Locate every blood parasite and identify its species.
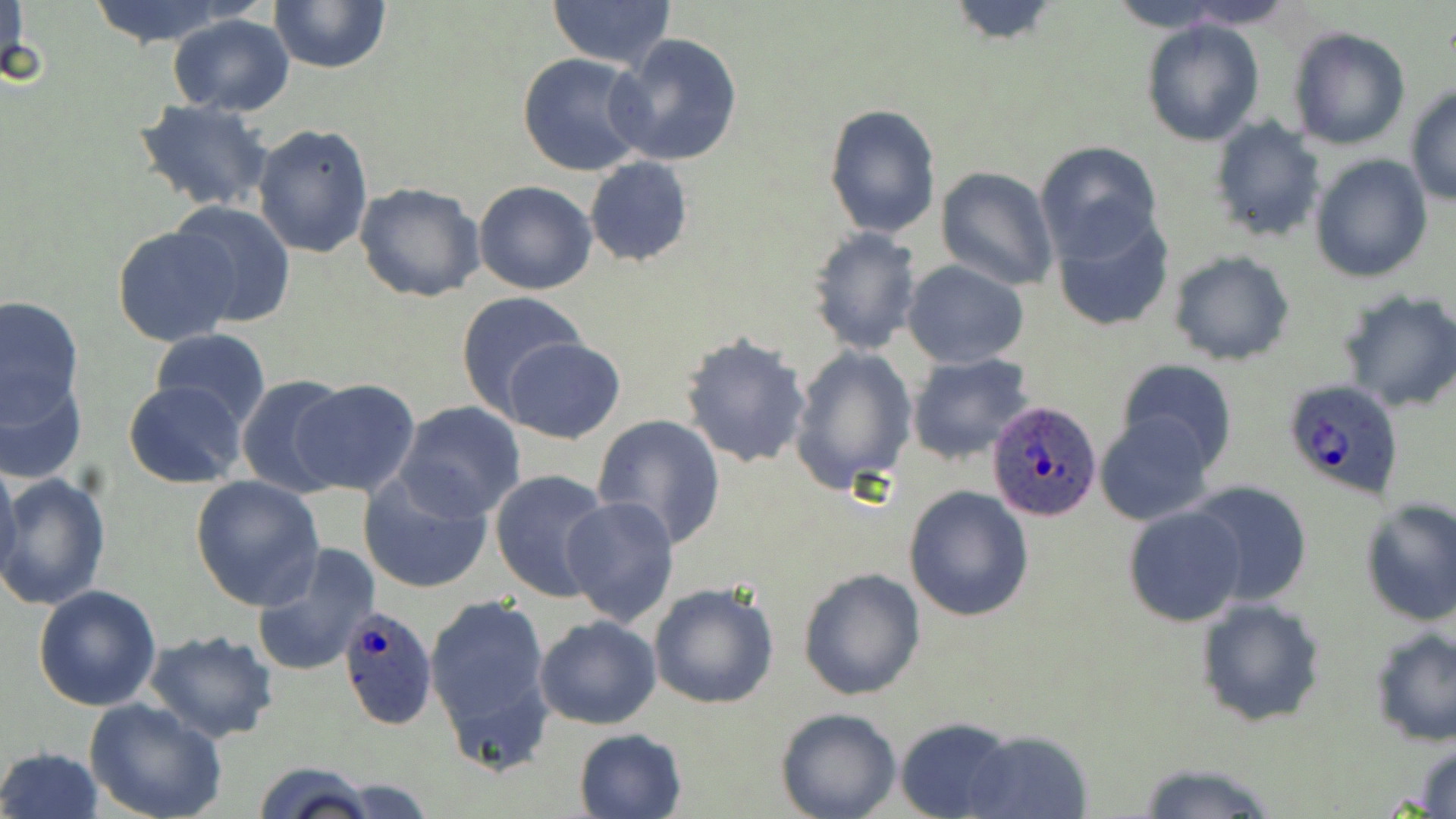
Approximate bounding boxes as (x1, y1, x2, y2) in pixels.
Plasmodium ovale-infected red blood cells: (1279, 378, 1407, 501), (987, 401, 1102, 524), (336, 605, 438, 730).
No Plasmodium falciparum, Plasmodium malariae, Plasmodium vivax, Babesia divergens, or Trypanosoma brucei observed.

{
  "slide_level_diagnosis": "Plasmodium ovale",
  "field_of_view": "single",
  "stain": "May-Grünwald-Giemsa",
  "uninfected_red_blood_cell_locations": "approximate bounding boxes as (x1, y1, x2, y2) in pixels: (1, 0, 32, 93), (85, 0, 238, 48), (268, 0, 392, 73), (545, 0, 677, 71), (942, 0, 1063, 45), (1103, 0, 1237, 33), (1171, 0, 1300, 30), (168, 14, 296, 116), (1141, 19, 1264, 145), (1288, 26, 1411, 150), (609, 33, 743, 167), (517, 51, 650, 176), (1404, 85, 1456, 205), (133, 99, 273, 212), (824, 103, 941, 237), (1207, 116, 1325, 243), (251, 122, 375, 259), (1035, 141, 1163, 264), (1309, 154, 1433, 283), (584, 156, 693, 267), (936, 166, 1058, 291), (355, 181, 487, 302), (473, 181, 598, 295), (169, 200, 296, 328), (1049, 209, 1176, 334), (112, 225, 241, 347), (806, 227, 921, 355), (1169, 252, 1295, 366), (902, 260, 1030, 367), (1338, 288, 1456, 414), (455, 291, 587, 417), (0, 293, 85, 429), (149, 329, 270, 430), (679, 331, 814, 470), (504, 337, 625, 445), (789, 344, 916, 493), (906, 353, 1035, 464), (1117, 358, 1238, 469), (1, 369, 88, 485), (237, 373, 352, 499), (289, 379, 422, 498), (123, 380, 246, 488), (397, 401, 525, 521), (1095, 411, 1216, 524), (591, 413, 727, 550), (0, 452, 22, 593), (357, 470, 492, 596), (491, 470, 615, 602), (0, 473, 112, 612), (190, 475, 325, 612), (1185, 481, 1314, 607), (904, 484, 1034, 622), (561, 494, 681, 627), (1358, 497, 1456, 626), (1124, 505, 1248, 627), (251, 544, 381, 676), (797, 568, 925, 700), (648, 579, 781, 709), (33, 585, 162, 712), (425, 594, 554, 762), (1195, 596, 1327, 728), (534, 614, 661, 729), (1368, 627, 1456, 747), (143, 629, 280, 745), (85, 699, 228, 819), (775, 707, 902, 819), (896, 717, 1018, 819), (574, 727, 688, 819), (963, 730, 1094, 819), (1412, 740, 1456, 817), (0, 746, 103, 819), (251, 761, 376, 819), (1132, 761, 1284, 819)",
  "magnification": "1000x",
  "image_size": "1456×819 pixels",
  "preparation": "thin blood film",
  "modality": "optical microscopy"
}